Evaluate for Plasmodium parasites.
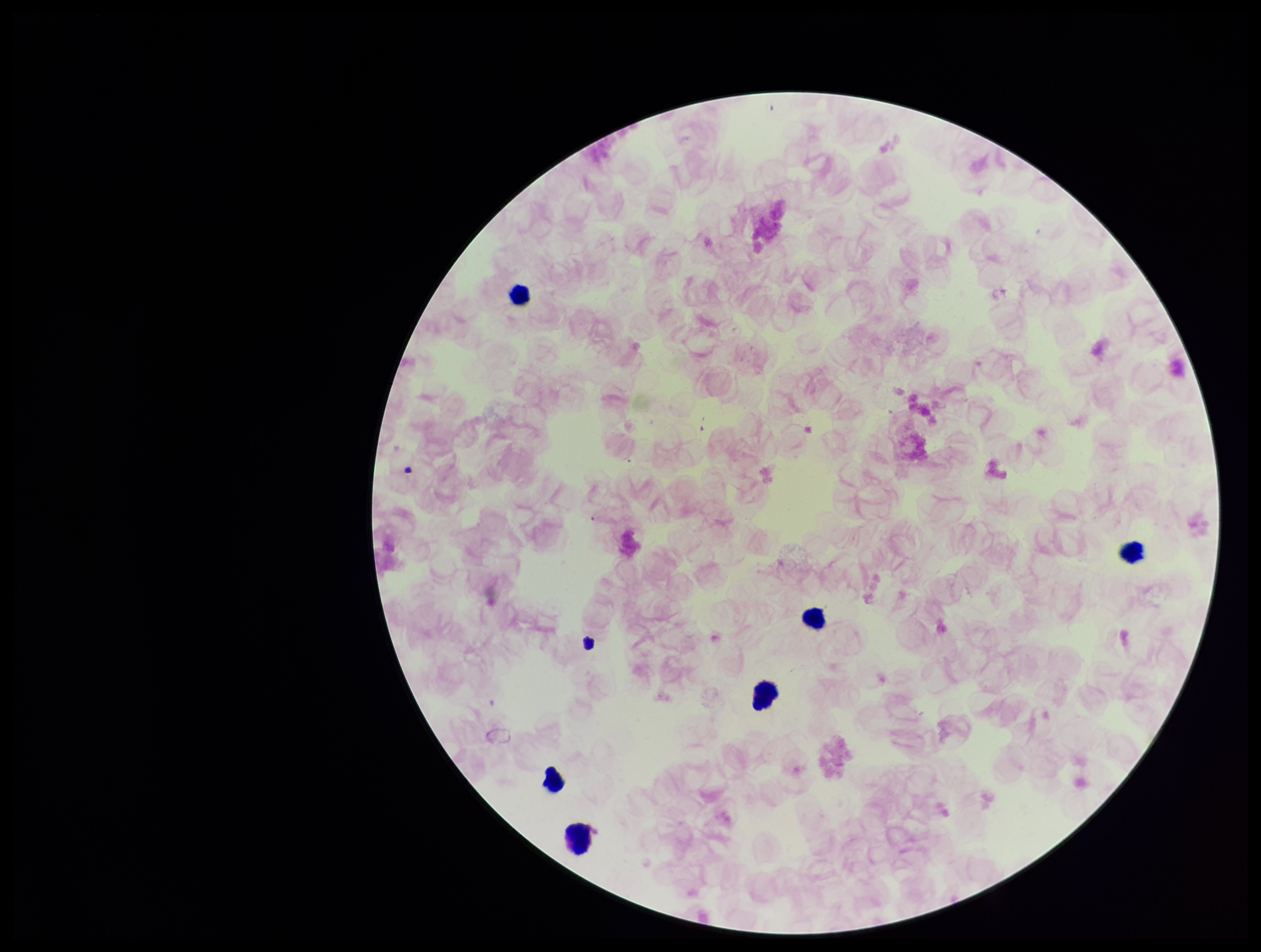
None detected.

preparation = thick smear
parasite count = 0
capture = smartphone photograph through the microscope eyepiece
field of view = single
patient malaria status = negative
leukocyte count = 6
stain = Giemsa
image size = 1261×952 pixels